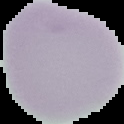

Image is 124×124 pixels. Malaria status: uninfected. Segmented cell region on a black background. From a thin blood smear.